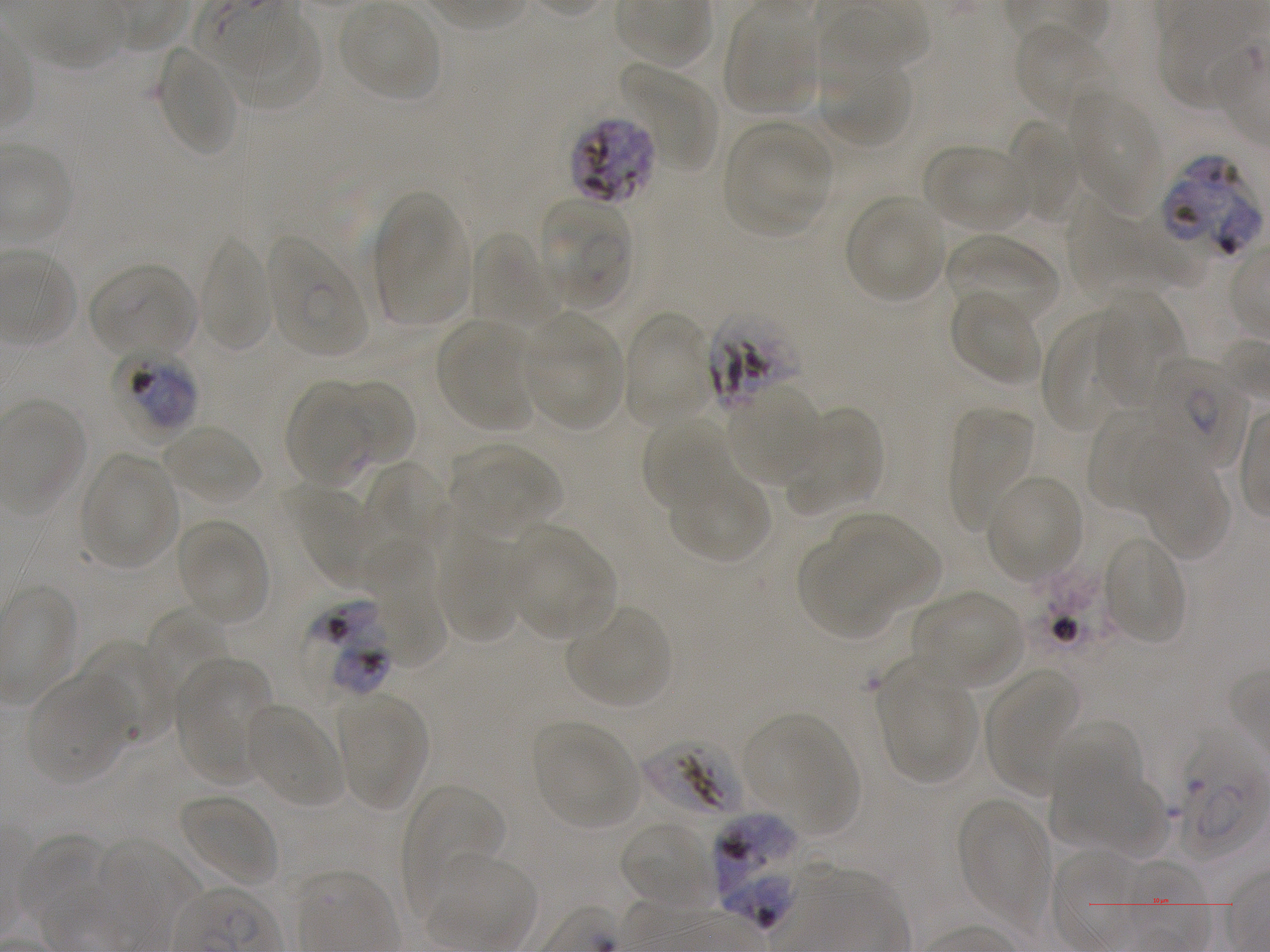
Not every red blood cell is marked. A life-cycle stage — or a range of stages, where the recorded stages span more than one — follows each staged infected red blood cell.
field of view = one from this slide
culture = static in-vitro Plasmodium falciparum strain NF54
locations of infected red blood cells = approximate bounding boxes as {x1, y1, x2, y2} in pixels: {570, 117, 658, 206}; {1162, 158, 1264, 257}; {537, 198, 633, 310} late ring; {266, 233, 368, 357} ring; {111, 349, 199, 436} late trophozoite to early schizont; {1150, 357, 1247, 469} early ring to early trophozoite; {330, 640, 397, 699} late trophozoite to late schizont; {1169, 729, 1266, 860}; {713, 813, 805, 925}
preparation = thin blood smear
donor blood group = A+
locations of uninfected red blood cells = approximate bounding boxes as {x1, y1, x2, y2} in pixels: {725, 8, 819, 114}, {229, 10, 323, 112}, {1013, 20, 1108, 121}, {158, 45, 239, 158}, {623, 62, 719, 172}, {820, 62, 916, 148}, {1069, 92, 1161, 206}, {1003, 119, 1081, 221}, {723, 121, 834, 238}, {925, 145, 1029, 232}, {373, 194, 470, 326}, {845, 196, 947, 303}, {1069, 198, 1177, 299}, {472, 231, 558, 330}, {946, 233, 1060, 330}, {199, 235, 273, 354}, {88, 264, 196, 358}, {948, 289, 1042, 387}, {1096, 301, 1186, 408}, {1040, 310, 1129, 433}, {623, 311, 713, 424}, {523, 315, 624, 430}, {437, 319, 535, 431}, {332, 378, 416, 467}, {285, 384, 375, 489}, {727, 388, 825, 487}, {949, 404, 1035, 531}, {784, 405, 883, 519}, {1088, 407, 1173, 513}, {642, 414, 729, 513}, {160, 423, 263, 507}, {451, 446, 560, 536}, {78, 453, 180, 571}, {364, 461, 449, 550}, {1145, 462, 1232, 561}, {669, 468, 771, 564}, {986, 475, 1084, 582}, {292, 490, 386, 590}, {826, 514, 939, 619}, {176, 520, 269, 624}, {510, 530, 616, 640}, {436, 533, 526, 643}, {1103, 536, 1187, 645}, {798, 537, 896, 640}, {369, 544, 445, 668}, {915, 591, 1023, 689}, {566, 606, 671, 709}, {142, 607, 229, 710}, {81, 641, 174, 742}, {877, 656, 979, 785}, {175, 663, 269, 782}, {985, 666, 1081, 790}, {26, 673, 135, 785}, {337, 697, 427, 809}, {245, 703, 343, 807}, {746, 715, 856, 826}, {532, 720, 641, 830}, {1047, 723, 1143, 820}, {1052, 766, 1161, 856}, {402, 783, 507, 901}, {178, 793, 278, 889}, {958, 799, 1050, 923}, {619, 819, 714, 909}, {13, 834, 107, 927}, {95, 839, 199, 926}, {428, 852, 537, 950}
stain = Giemsa
locations of red blood cells of indeterminate infection status = approximate bounding boxes as {x1, y1, x2, y2} in pixels: {708, 309, 805, 415}, {303, 595, 386, 646}, {640, 738, 744, 819}
image size = 1270×952 pixels
objective = 100x, oil immersion, numerical aperture 1.25